Locate every blood parasite and identify its species.
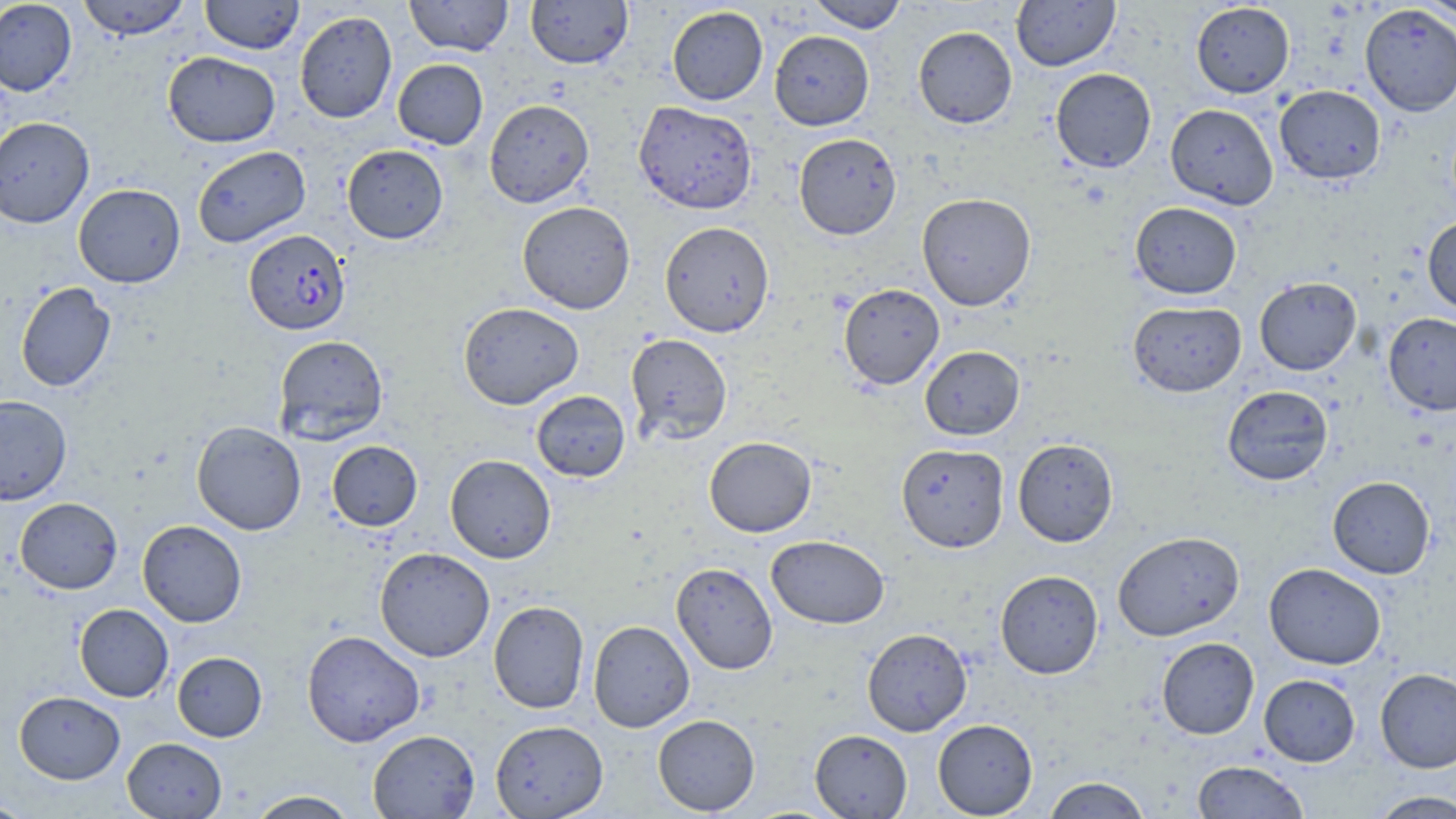

Approximate bounding boxes as [x1, y1, x2, y2] in pixels.
Plasmodium falciparum-infected red blood cells: [244, 229, 350, 335].
No Plasmodium ovale, Plasmodium malariae, Plasmodium vivax, Babesia divergens, or Trypanosoma brucei observed.

slide-level diagnosis = Plasmodium falciparum
magnification = 1000x
field of view = single
stain = May-Grünwald-Giemsa
preparation = thin blood film
image size = 1456×819 pixels
modality = optical microscopy
uninfected red blood cell locations = approximate bounding boxes as [x1, y1, x2, y2] in pixels: [0, 0, 77, 96], [76, 0, 192, 40], [200, 0, 305, 54], [404, 0, 513, 56], [526, 0, 633, 69], [807, 0, 908, 32], [1011, 0, 1120, 71], [1418, 0, 1455, 23], [1191, 2, 1295, 98], [1360, 4, 1456, 116], [667, 6, 768, 105], [294, 10, 397, 123], [913, 26, 1017, 128], [769, 30, 874, 130], [163, 51, 280, 147], [393, 59, 488, 149], [1050, 68, 1156, 173], [1274, 85, 1386, 184], [484, 99, 594, 208], [633, 101, 757, 214], [1165, 103, 1278, 209], [0, 116, 94, 228], [794, 133, 901, 239], [342, 144, 448, 244], [192, 145, 310, 247], [73, 183, 185, 288], [917, 192, 1036, 311], [517, 201, 635, 314], [1130, 201, 1242, 299], [1422, 216, 1456, 315], [660, 221, 774, 337], [1254, 277, 1361, 375], [15, 282, 116, 392], [838, 283, 946, 389], [458, 301, 584, 410], [1128, 301, 1246, 397], [1383, 312, 1456, 415], [625, 333, 733, 445], [273, 335, 388, 445], [920, 345, 1025, 440], [1222, 385, 1333, 486], [531, 390, 630, 482], [0, 395, 72, 505], [191, 421, 306, 535], [704, 436, 816, 537], [1013, 438, 1119, 547], [327, 440, 423, 531], [896, 443, 1009, 553], [445, 454, 556, 563], [1328, 476, 1435, 578], [15, 497, 123, 594], [137, 519, 247, 627], [1112, 531, 1245, 641], [766, 535, 890, 629], [374, 547, 495, 662], [671, 562, 778, 675], [1263, 562, 1386, 669], [995, 570, 1103, 679], [488, 600, 589, 714], [74, 604, 173, 702], [588, 620, 695, 732], [862, 628, 972, 736], [302, 630, 425, 747], [1157, 636, 1259, 739], [172, 651, 267, 742], [1375, 668, 1456, 773], [1259, 674, 1360, 766], [14, 690, 125, 783], [652, 714, 760, 815], [933, 718, 1038, 818], [490, 720, 608, 818], [367, 729, 480, 818], [810, 729, 912, 818], [122, 737, 227, 819], [1192, 760, 1308, 818], [1043, 776, 1151, 818], [1367, 789, 1456, 818], [246, 790, 360, 819], [0, 797, 34, 819]